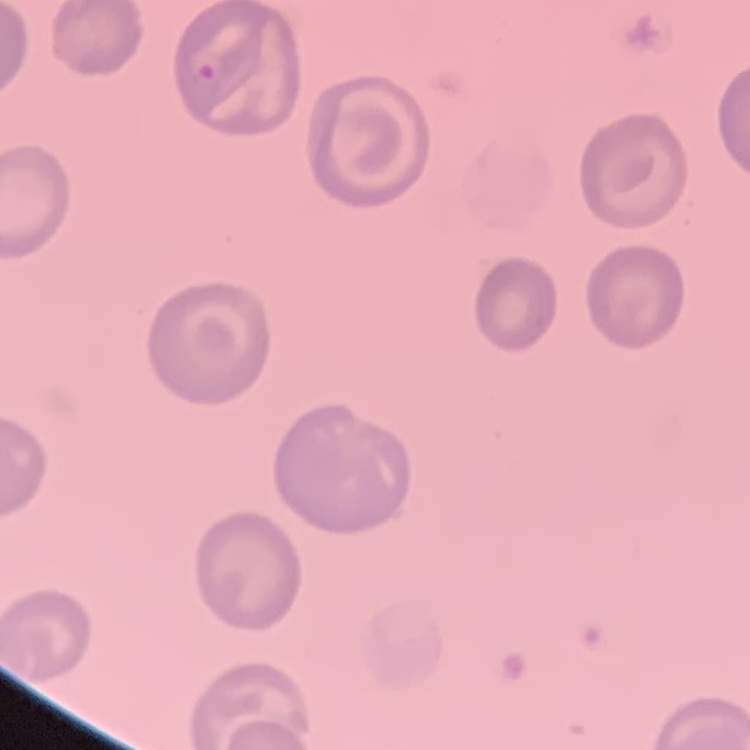

The erythrocytes exhibit no rouleaux formation. Field's or Giemsa stain. Thin blood smear. Square crop of a larger photomicrograph.